Classify this cell by malaria status.
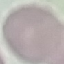

It is uninfected.

Automatically extracted cell patch, resized to 64 × 64 pixels. Giemsa-stained preparation. Thin blood smear. Photographed with a smartphone camera at the microscope eyepiece.